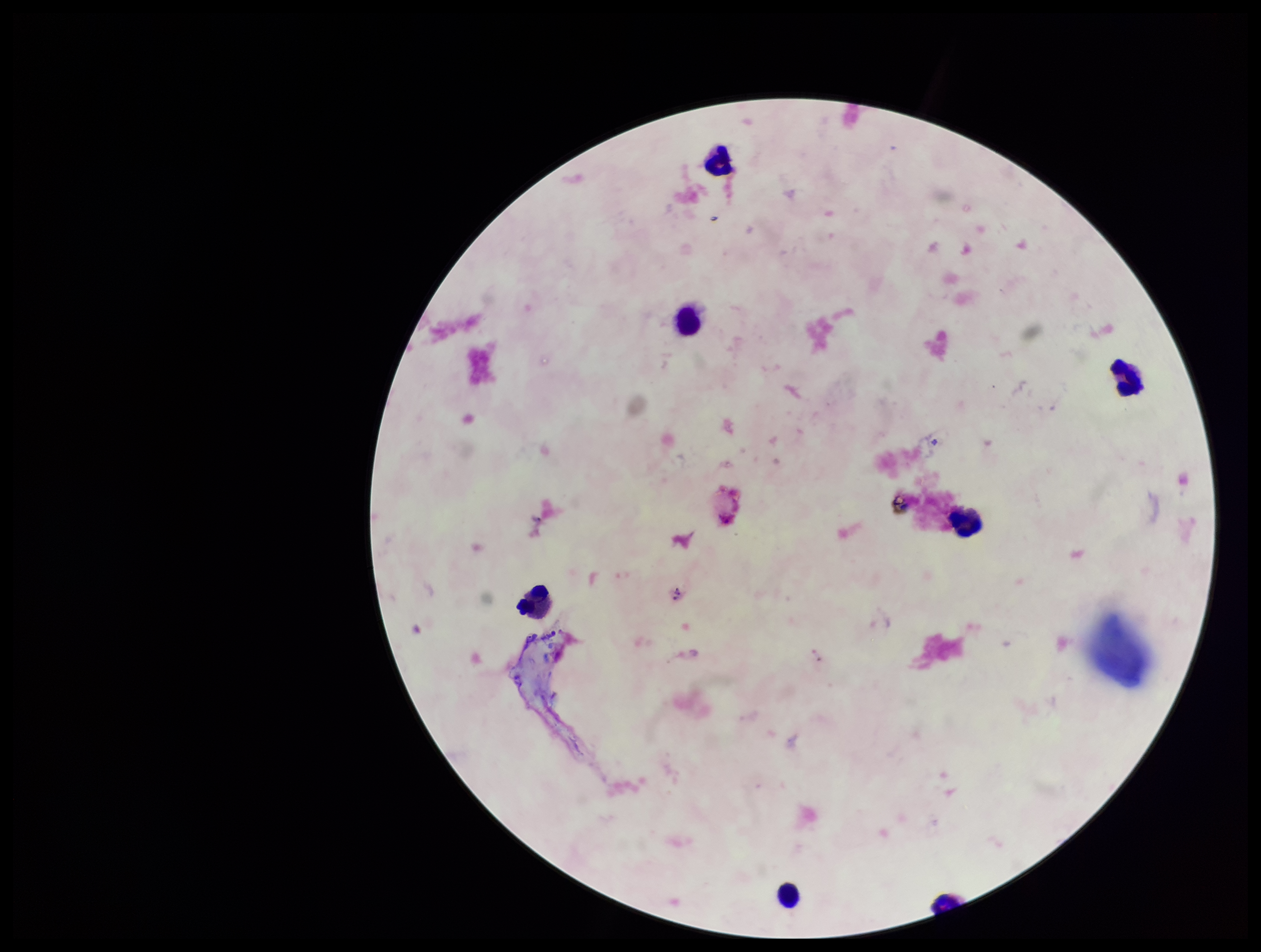
Summary:
  - Parasite count: 0
  - Plasmodium parasites: none detected
  - Image size: 1261×952 pixels
  - Preparation: thick smear
  - Stain: Giemsa
  - Leukocyte count: 7
  - Patient malaria status: negative
  - Field of view: single
  - Capture: smartphone photograph through the microscope eyepiece